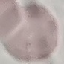
Summary:
  - Malaria status: uninfected
  - Stain: Giemsa
  - Preparation: thin blood smear
  - Image type: cell patch, automatically extracted from a larger field of view and resized to 64 × 64 pixels
  - Capture: smartphone camera at the microscope eyepiece